Report the malaria status of this cell.
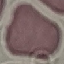

It is uninfected.

Thin smear of blood. Giemsa-stained preparation. Automatically extracted cell patch, resized to 64 × 64 pixels. Photographed with a smartphone camera at the microscope eyepiece.